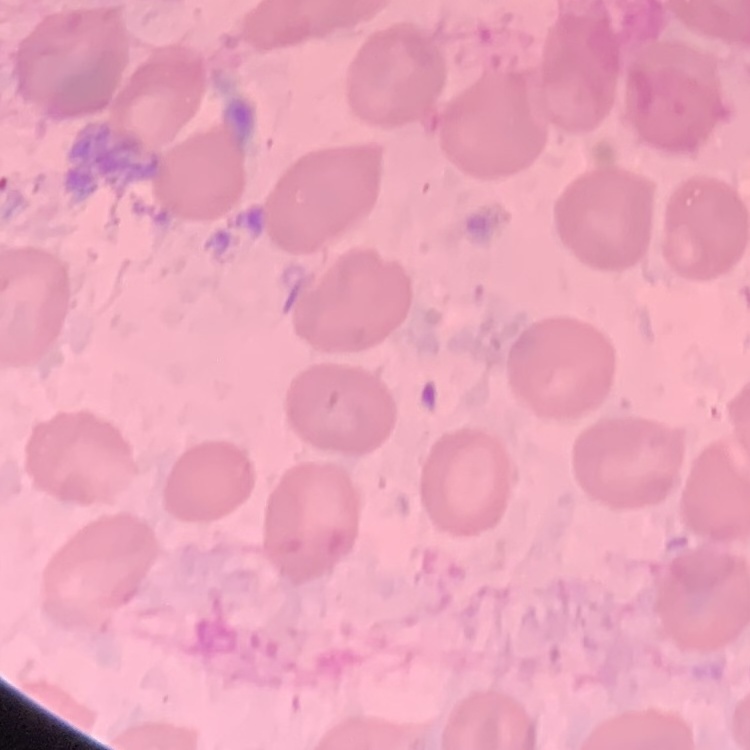
Summary:
  - Erythrocyte morphology: no rouleaux formation
  - Image type: square crop of a larger photomicrograph
  - Stain: Field's or Giemsa
  - Preparation: thin blood film